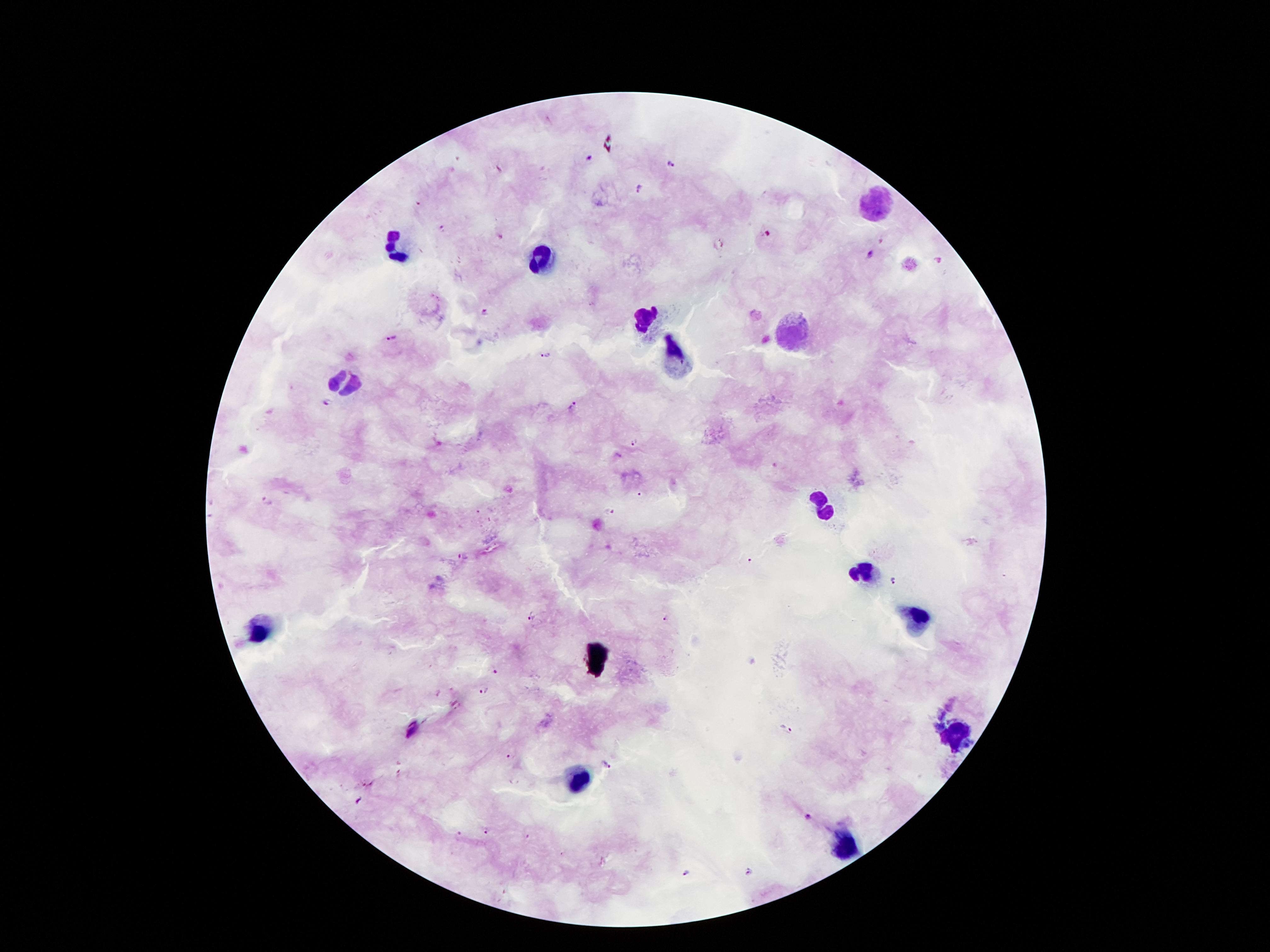

Approximate centers as (x, y) in pixels. Malaria parasite locations: (589, 158), (672, 163), (641, 187), (442, 227), (768, 234), (870, 253), (937, 260), (486, 312), (391, 337), (545, 356), (327, 402), (573, 406), (634, 443), (639, 491), (267, 500), (609, 512), (463, 555), (751, 559), (893, 582), (531, 618), (667, 619), (492, 669), (483, 690), (788, 730), (510, 756), (604, 765), (808, 815), (486, 830), (459, 837), (747, 871), (688, 874). Leukocyte locations: (872, 205), (398, 245), (543, 258), (646, 321), (794, 335), (674, 357), (347, 382), (826, 504), (861, 573), (920, 616), (263, 631), (956, 738), (581, 779), (846, 845). 100x magnification. Image is 1270×952 pixels. Thick blood smear. Photographed through the microscope eyepiece with a smartphone camera. Giemsa-stained preparation. One field from this slide. Patient malaria status: positive for Plasmodium falciparum.